Locate every leukocyte (white blood cell).
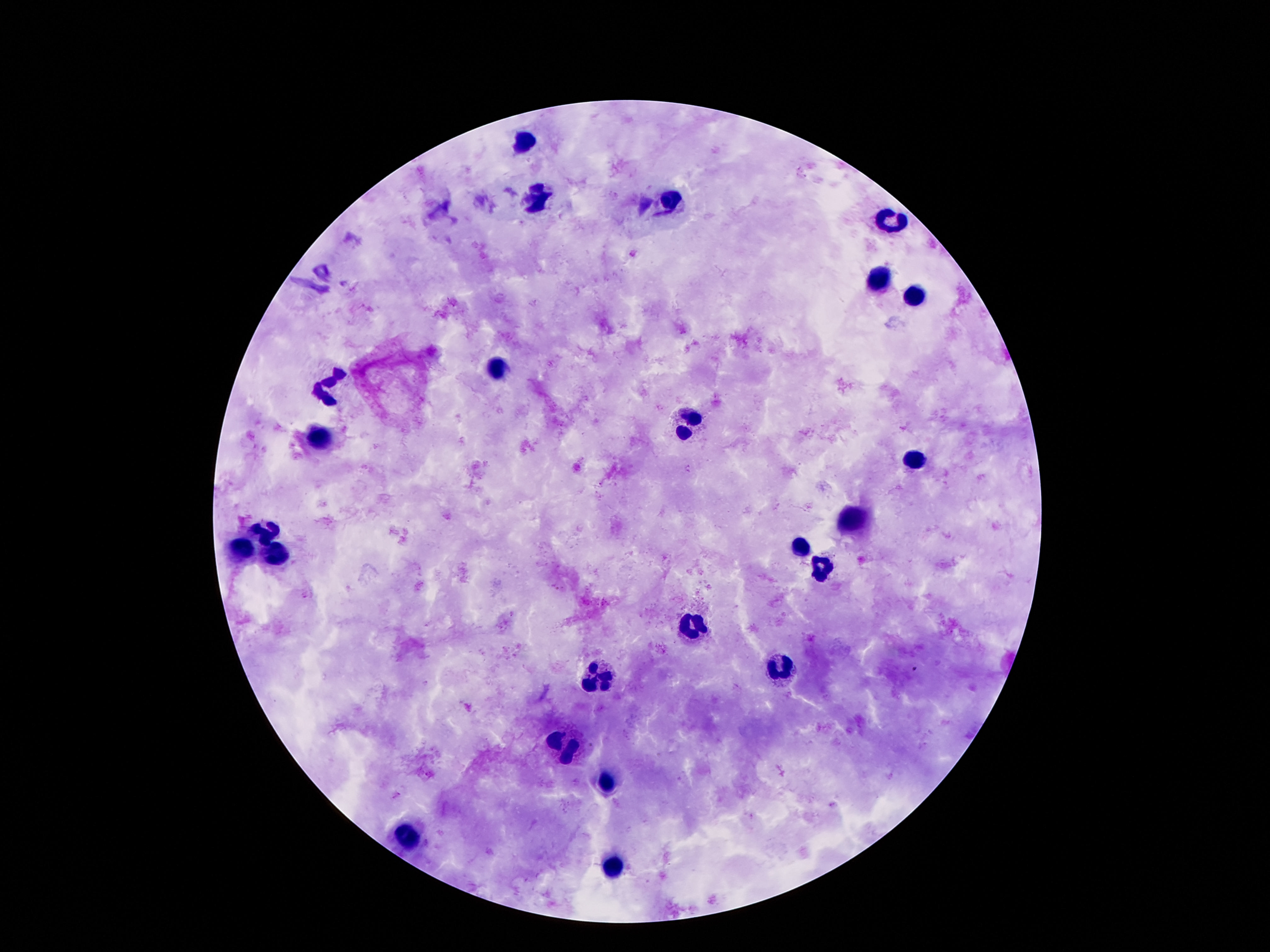

Approximate centers as (x, y) in pixels.
Leukocytes: (522, 142), (538, 198), (669, 206), (892, 220), (879, 278), (914, 296), (498, 367), (330, 383), (688, 427), (323, 437), (913, 460), (853, 521), (261, 532), (240, 548), (799, 548), (274, 553), (823, 569), (694, 627), (779, 667), (596, 674), (566, 747), (604, 785), (405, 838), (611, 868).

Patient malaria status: not infected. 100x magnification. Thick peripheral-blood smear. Giemsa stain. Smartphone photograph taken through the microscope eyepiece. Image is 1270×952 pixels. One field from this slide.